Locate every blood parasite and identify its species.
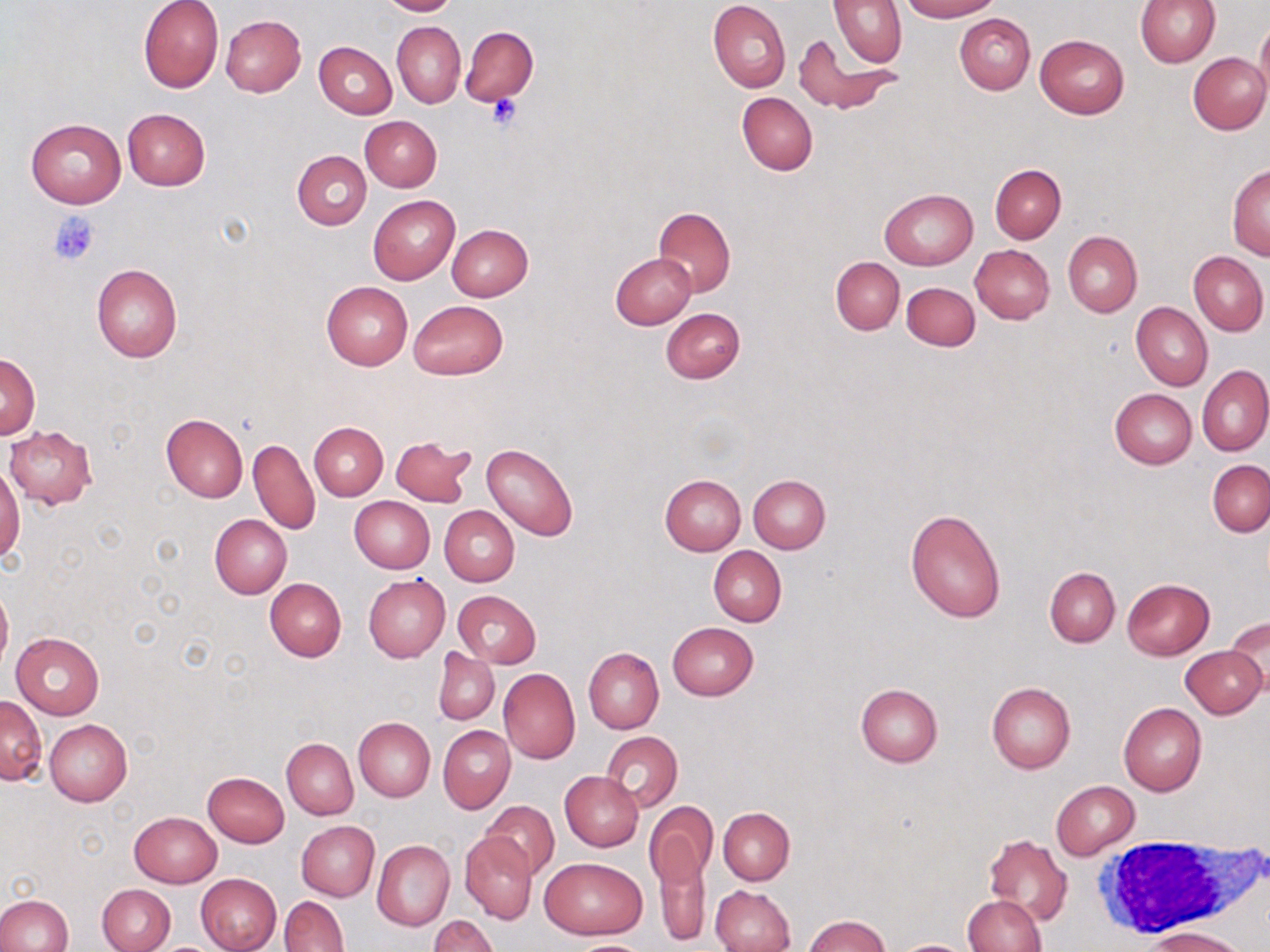

No blood parasites seen.

Summary:
  - Coordinate format: approximate bounding boxes as (x1, y1, x2, y2) in pixels
  - Platelet locations: (487, 94, 522, 129), (47, 211, 100, 264)
  - White blood cell locations: (1092, 835, 1255, 939)
  - Uninfected red blood cell locations: (138, 0, 224, 93), (377, 0, 457, 17), (708, 0, 790, 93), (829, 0, 906, 67), (900, 0, 999, 21), (1135, 0, 1220, 68), (954, 13, 1035, 94), (220, 14, 306, 97), (1256, 18, 1270, 102), (392, 21, 464, 107), (462, 26, 538, 106), (796, 34, 900, 117), (1036, 34, 1129, 118), (314, 42, 397, 119), (1186, 52, 1269, 135), (737, 92, 818, 176), (122, 109, 209, 190), (359, 116, 442, 191), (26, 118, 125, 208), (292, 150, 372, 229), (990, 163, 1066, 243), (1226, 165, 1270, 260), (879, 188, 977, 269), (368, 195, 460, 284), (654, 207, 736, 296), (446, 224, 533, 302), (1063, 231, 1142, 317), (970, 245, 1054, 323), (1188, 250, 1268, 336), (611, 252, 697, 329), (831, 257, 904, 334), (92, 264, 182, 362), (321, 281, 412, 370), (902, 281, 980, 350), (408, 299, 509, 380), (1131, 302, 1212, 390), (660, 308, 744, 383), (0, 351, 40, 439), (1198, 366, 1270, 456), (1110, 389, 1196, 469), (161, 413, 249, 501), (310, 422, 387, 499), (5, 426, 97, 508), (249, 437, 320, 535), (389, 437, 475, 506), (482, 442, 578, 541), (1208, 460, 1270, 536), (0, 467, 24, 565), (660, 474, 745, 555), (748, 474, 831, 553), (350, 496, 434, 573), (440, 505, 519, 586), (906, 507, 1007, 624), (209, 514, 292, 600), (709, 545, 787, 626), (1045, 567, 1120, 646), (364, 574, 451, 663), (265, 577, 347, 661), (1122, 578, 1215, 659), (0, 582, 12, 674), (454, 590, 541, 667), (1226, 617, 1269, 690), (667, 622, 759, 701), (10, 631, 105, 719), (1182, 645, 1267, 718), (433, 648, 499, 725), (583, 648, 663, 733), (499, 669, 580, 763), (986, 682, 1076, 773), (855, 683, 943, 766), (1, 694, 46, 784), (1118, 702, 1206, 796), (353, 717, 435, 801), (44, 719, 132, 807), (439, 725, 515, 812), (601, 731, 683, 812), (283, 738, 357, 819), (569, 749, 677, 834), (202, 772, 289, 848), (560, 772, 643, 851), (1052, 781, 1140, 859), (482, 800, 560, 880), (647, 806, 715, 937), (718, 807, 795, 884), (129, 812, 221, 888), (297, 821, 379, 900), (460, 831, 536, 924), (983, 833, 1071, 927), (372, 839, 455, 931), (538, 856, 648, 939), (196, 873, 282, 952), (98, 884, 174, 952), (709, 884, 794, 952), (0, 895, 72, 951), (962, 895, 1046, 952), (280, 896, 348, 952), (802, 914, 892, 952), (429, 915, 499, 952), (1145, 925, 1250, 952), (566, 939, 652, 952), (898, 940, 970, 952)
  - Slide-level diagnosis: negative for blood parasites
  - Preparation: thin blood film
  - Stain: May-Grünwald-Giemsa
  - Field of view: single
  - Modality: optical microscopy
  - Magnification: 1000x
  - Image size: 1270×952 pixels